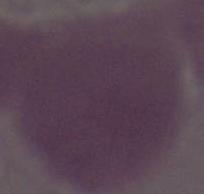
Micrograph. Captured at 1000x magnification. An erythrocyte is shown.